State which parasite is depicted.
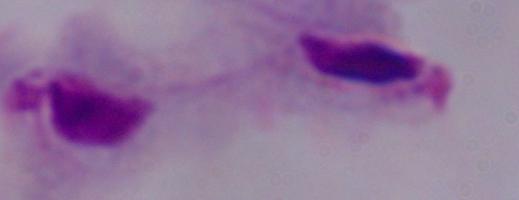

This is a trichomonad.

Photomicrograph. 1000x magnification.